Evaluate for Plasmodium parasites.
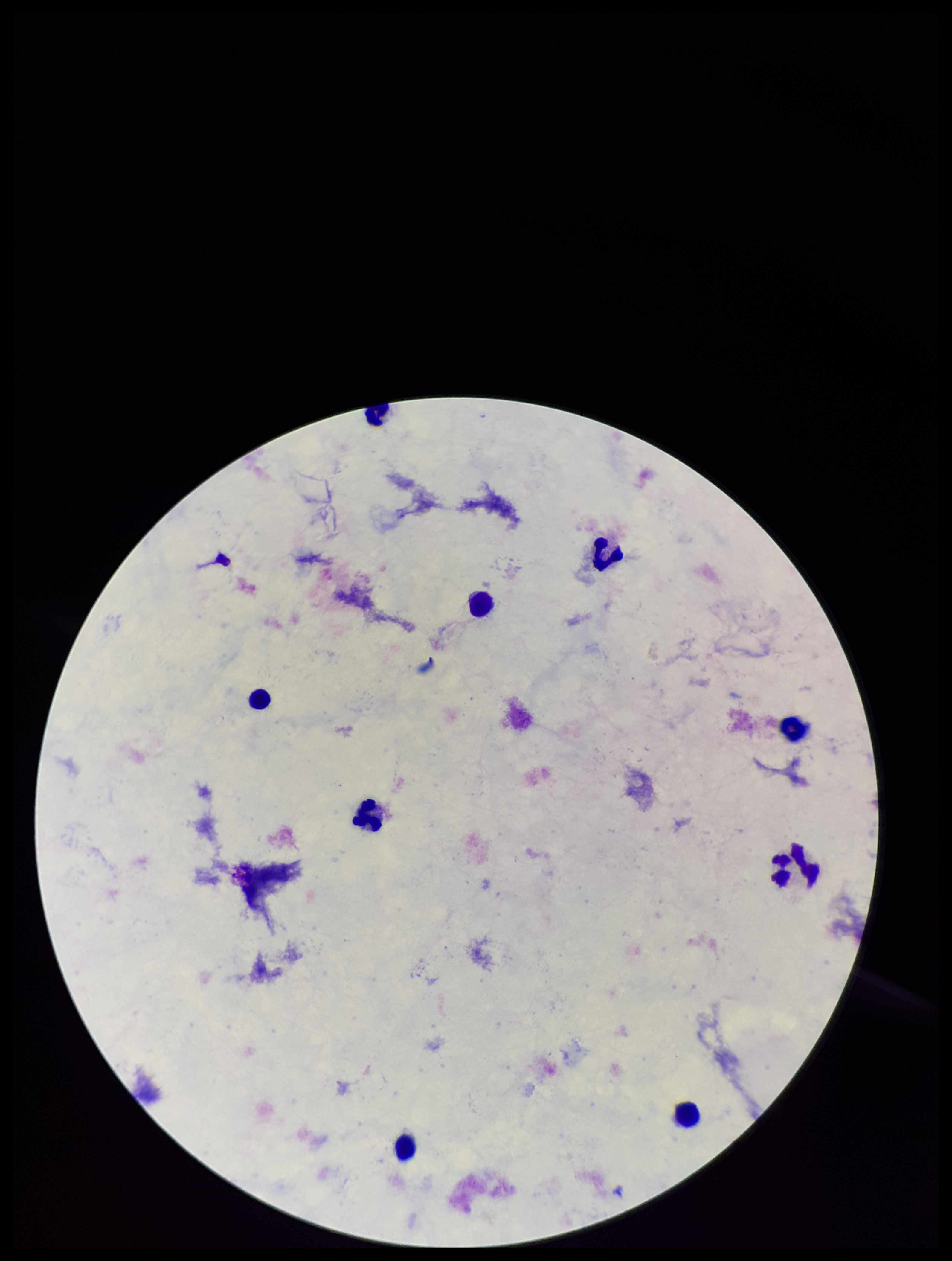

None identified.

parasite count = 0
leukocyte count = 9
capture = smartphone photograph through the microscope eyepiece
preparation = thick smear
stain = Giemsa
patient malaria status = negative
image size = 952×1261 pixels
field of view = single